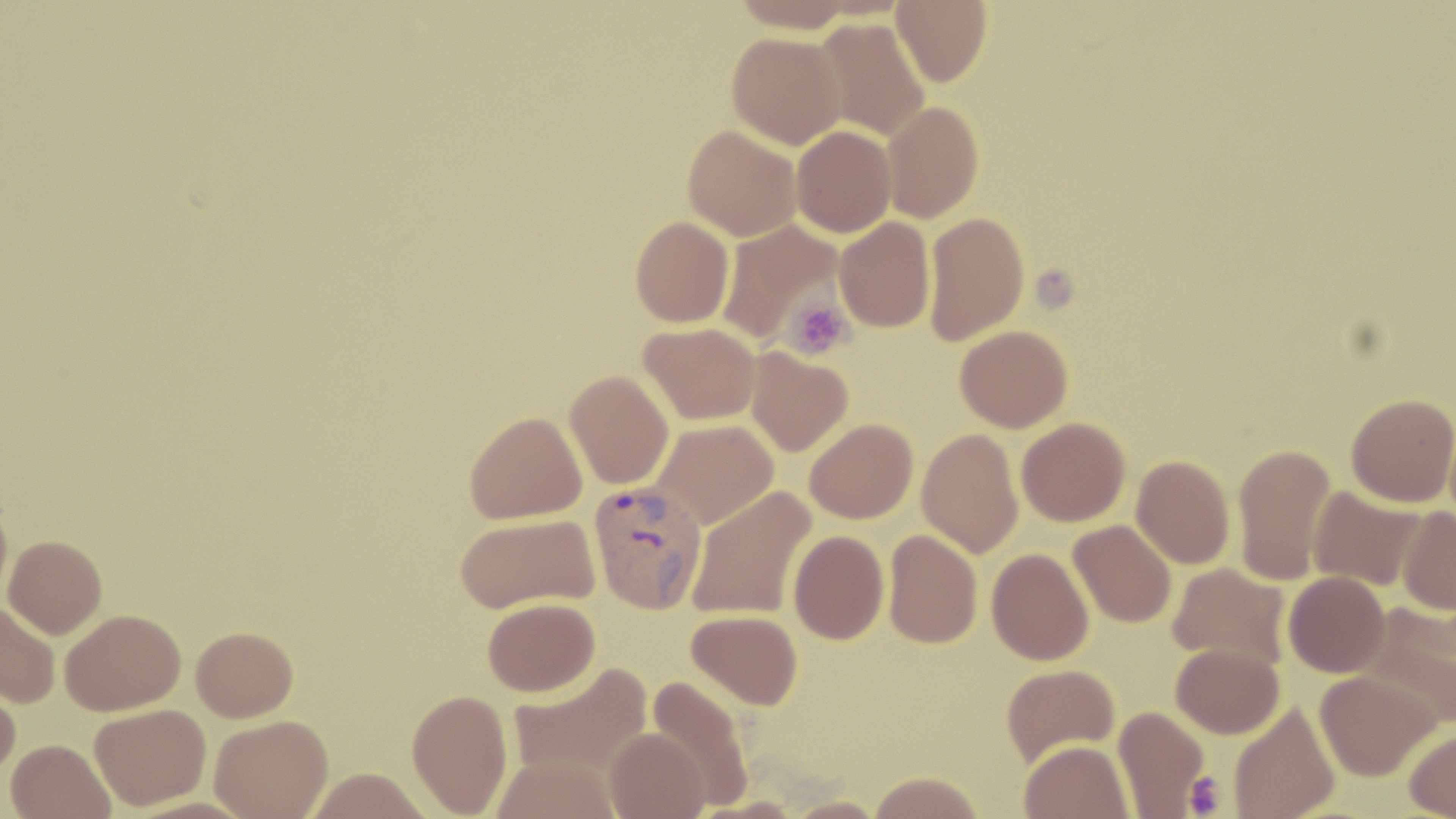 Approximate bounding boxes as (x1,y1)-(x2,y2) corner pairs in pixels. Uninfected red blood cell locations: (731,0)-(858,33), (891,0)-(991,86), (813,18)-(931,141), (727,31)-(846,149), (881,100)-(984,222), (683,124)-(801,241), (790,125)-(896,238), (923,211)-(1029,344), (630,216)-(734,327), (834,216)-(935,332), (718,220)-(843,345), (639,322)-(760,425), (955,324)-(1073,432), (746,347)-(853,456), (565,370)-(674,489), (1346,394)-(1456,507), (464,411)-(587,523), (1016,417)-(1130,526), (805,418)-(918,523), (653,420)-(778,529), (917,427)-(1023,557), (1232,443)-(1336,585), (1132,455)-(1235,568), (688,485)-(816,620), (1308,486)-(1426,591), (0,491)-(13,608), (1397,506)-(1456,615), (455,513)-(600,614), (1068,519)-(1177,627), (883,529)-(982,648), (788,530)-(889,644), (3,535)-(107,638), (987,547)-(1094,665), (1167,563)-(1290,669), (1283,571)-(1390,677), (482,597)-(600,696), (0,600)-(60,707), (1358,603)-(1456,728), (59,608)-(185,715), (686,609)-(803,709), (191,625)-(298,721), (1171,643)-(1284,738), (507,662)-(652,784), (1001,663)-(1119,766), (1314,670)-(1440,781), (0,673)-(21,780), (646,674)-(755,809), (407,688)-(513,817), (1229,700)-(1341,819), (89,704)-(210,810), (1113,705)-(1209,817), (209,715)-(333,819), (604,727)-(710,818), (1404,727)-(1456,818), (6,739)-(115,819), (1019,739)-(1134,819), (488,755)-(621,819), (304,766)-(433,818), (868,772)-(984,818), (783,796)-(886,819). Platelet locations: (1034,267)-(1078,318), (783,297)-(854,360), (1185,771)-(1227,816). Plasmodium vivax-infected red blood cell locations: (588,480)-(708,614). Slide-level diagnosis: Plasmodium vivax. Optical microscopy. One field of a larger specimen. May-Grünwald-Giemsa stain. Image is 1456×819 pixels. Captured at 1000x magnification. Thin blood film.